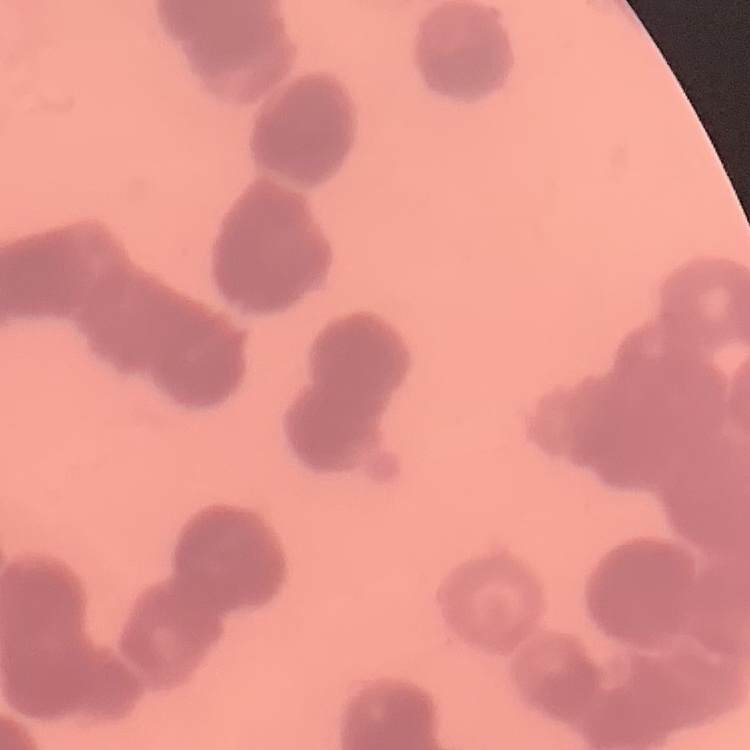

erythrocyte morphology = rouleaux formation
stain = Field's or Giemsa
image type = one tile cut from a larger photomicrograph
preparation = thin blood smear